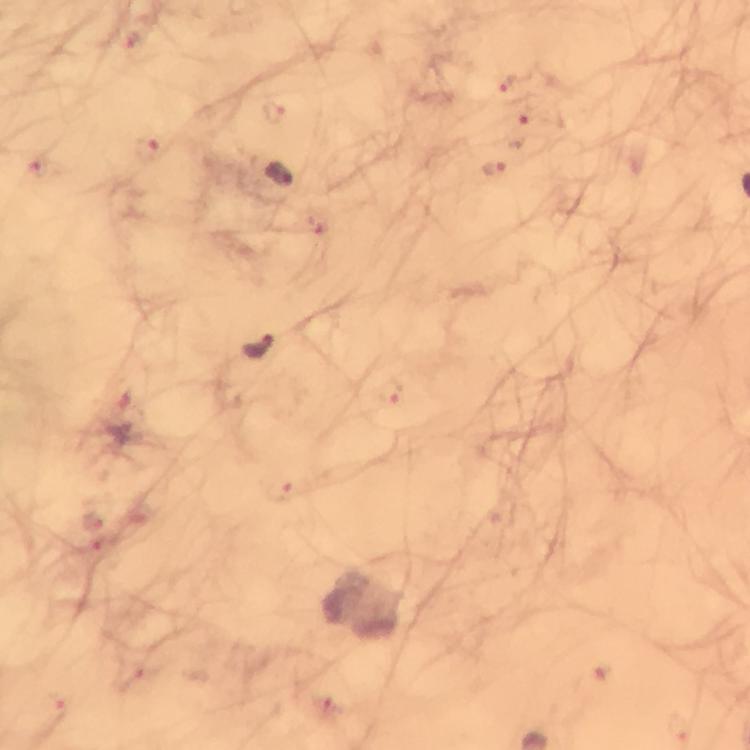

Approximate centers as [x, y] in pixels.
Summary:
  - Malaria parasite locations: [508, 85], [146, 151], [494, 168], [279, 176], [258, 348], [390, 391], [278, 491]
  - Image size: 750×750 pixels
  - Context: from a malaria diagnostic workup
  - Preparation: thick blood film
  - Capture: smartphone photograph through a microscope
  - Cropped from: a single field of view
  - Stain: Giemsa
  - Immersion oil: used
  - Magnification: 100x